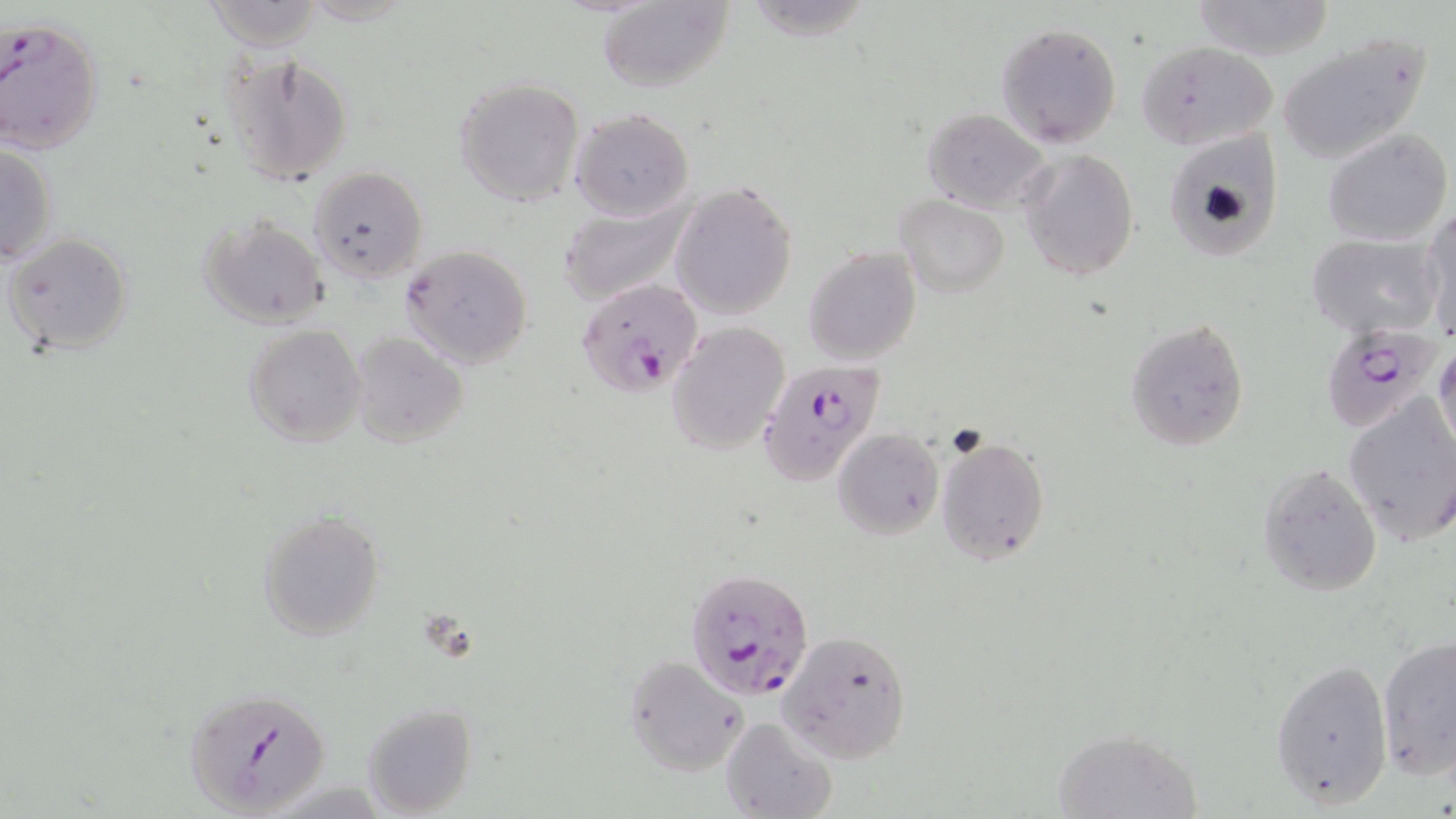
Summary:
  - Coordinate format: approximate bounding boxes as [x1, y1, x2, y2] in pixels
  - Uninfected red blood cell locations: [204, 0, 325, 49], [597, 0, 735, 93], [1188, 1, 1335, 59], [997, 22, 1122, 148], [1274, 28, 1433, 165], [1137, 40, 1279, 150], [218, 50, 356, 189], [453, 76, 584, 206], [922, 106, 1054, 215], [569, 108, 694, 223], [1323, 127, 1453, 246], [1164, 133, 1285, 262], [1, 143, 58, 265], [1019, 147, 1140, 282], [309, 166, 428, 284], [669, 180, 799, 322], [558, 194, 694, 307], [896, 196, 1010, 299], [1421, 208, 1456, 336], [198, 215, 330, 330], [4, 232, 134, 357], [1305, 232, 1443, 340], [399, 245, 533, 369], [804, 246, 921, 365], [1125, 317, 1252, 454], [667, 321, 791, 455], [243, 324, 365, 448], [350, 332, 469, 447], [1432, 341, 1456, 456], [1343, 395, 1456, 543], [832, 427, 943, 539], [934, 434, 1050, 568], [1257, 464, 1382, 598], [255, 509, 385, 642], [778, 631, 913, 763], [1376, 633, 1456, 780], [621, 655, 747, 778], [1270, 658, 1394, 809], [363, 704, 478, 817], [720, 716, 837, 819], [1052, 728, 1201, 818]
  - Plasmodium falciparum-infected red blood cell locations: [0, 18, 104, 153], [576, 278, 704, 395], [1320, 324, 1446, 432], [764, 350, 896, 492], [686, 566, 815, 702], [183, 685, 332, 817]
  - Slide-level diagnosis: Plasmodium falciparum
  - Preparation: thin blood film
  - Magnification: 1000x
  - Modality: light microscopy
  - Image size: 1456×819 pixels
  - Stain: May-Grünwald-Giemsa
  - Field of view: one of a larger specimen